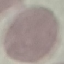 Result: no malaria parasites detected. Photographed with a smartphone camera at the microscope eyepiece. Giemsa stain. Thin smear of blood. Cell patch, automatically extracted from a larger field of view and resized to 64 × 64 pixels.